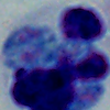
Micrograph. A white blood cell is shown. 1000x magnification.